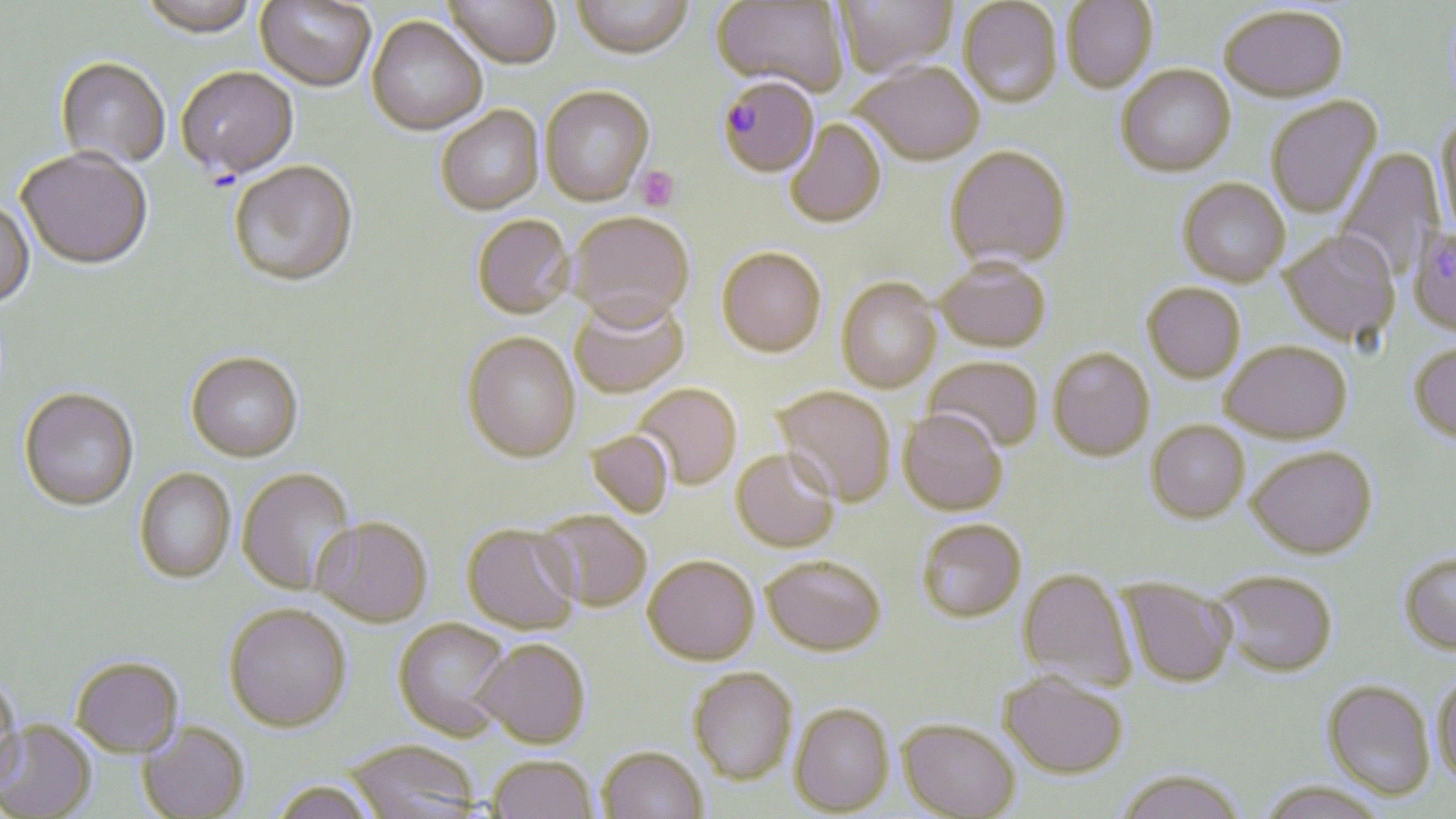
{
  "slide_level_diagnosis": "Plasmodium falciparum",
  "image_size": "1456×819 pixels",
  "field_of_view": "one of a larger specimen",
  "stain": "May-Grünwald-Giemsa",
  "plasmodium_falciparum_infected_red_blood_cell_locations": "approximate bounding boxes as [x1, y1, x2, y2] in pixels: [718, 78, 821, 179]",
  "magnification": "1000x",
  "uninfected_red_blood_cell_locations": "approximate bounding boxes as [x1, y1, x2, y2] in pixels: [255, 0, 375, 94], [444, 0, 560, 72], [571, 0, 693, 62], [712, 0, 849, 96], [835, 0, 956, 78], [1062, 0, 1157, 94], [138, 1, 259, 42], [958, 1, 1063, 109], [1218, 5, 1348, 103], [366, 19, 487, 138], [55, 61, 170, 170], [853, 63, 984, 166], [1116, 65, 1236, 178], [176, 68, 299, 182], [540, 89, 654, 208], [1266, 96, 1382, 219], [436, 108, 544, 217], [1434, 114, 1456, 237], [785, 120, 886, 229], [945, 146, 1072, 270], [1335, 148, 1445, 282], [16, 150, 153, 272], [229, 164, 358, 289], [1177, 179, 1290, 286], [0, 201, 35, 311], [569, 214, 694, 332], [472, 217, 575, 321], [1408, 226, 1456, 336], [1282, 230, 1401, 346], [716, 247, 827, 357], [936, 257, 1052, 352], [836, 278, 942, 392], [1142, 282, 1246, 382], [570, 296, 689, 400], [462, 334, 582, 465], [1221, 341, 1352, 442], [1408, 342, 1456, 444], [1048, 347, 1155, 460], [186, 354, 303, 465], [924, 356, 1044, 453], [634, 384, 742, 489], [773, 386, 896, 507], [19, 390, 139, 513], [898, 409, 1008, 515], [1146, 420, 1250, 522], [585, 430, 675, 518], [1248, 445, 1377, 558], [731, 448, 840, 553], [236, 468, 359, 596], [134, 469, 235, 584], [533, 511, 651, 612], [311, 517, 433, 628], [916, 518, 1027, 621], [461, 524, 580, 634], [1398, 551, 1456, 654], [643, 555, 759, 665], [761, 555, 886, 655], [1018, 567, 1137, 691], [1215, 569, 1338, 676], [1120, 578, 1237, 687], [223, 604, 351, 732], [393, 618, 513, 740], [473, 639, 590, 747], [70, 656, 184, 757], [688, 668, 798, 785], [998, 670, 1129, 779], [1431, 670, 1456, 789], [0, 675, 23, 792], [1321, 679, 1435, 799], [790, 703, 894, 815], [898, 717, 1021, 818], [0, 720, 97, 817], [137, 721, 250, 819], [344, 739, 482, 819], [597, 746, 708, 819], [486, 754, 599, 819], [1114, 768, 1246, 819], [269, 779, 379, 819], [1257, 780, 1391, 819]",
  "preparation": "thin blood smear",
  "platelet_locations": "approximate bounding boxes as [x1, y1, x2, y2] in pixels: [635, 166, 680, 211]",
  "modality": "optical microscopy"
}